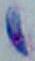
Toxoplasma gondii is seen. 1000x magnification. Photomicrograph.